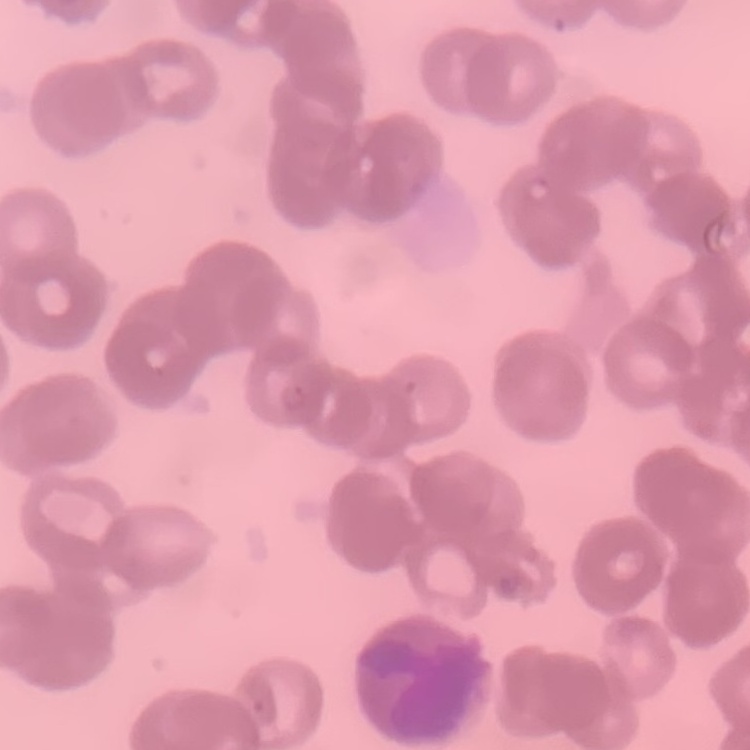

{
  "red_blood_cell_morphology": "rouleaux formation",
  "image_type": "one tile cut from a larger photomicrograph",
  "stain": "Field's or Giemsa",
  "preparation": "thin blood film"
}